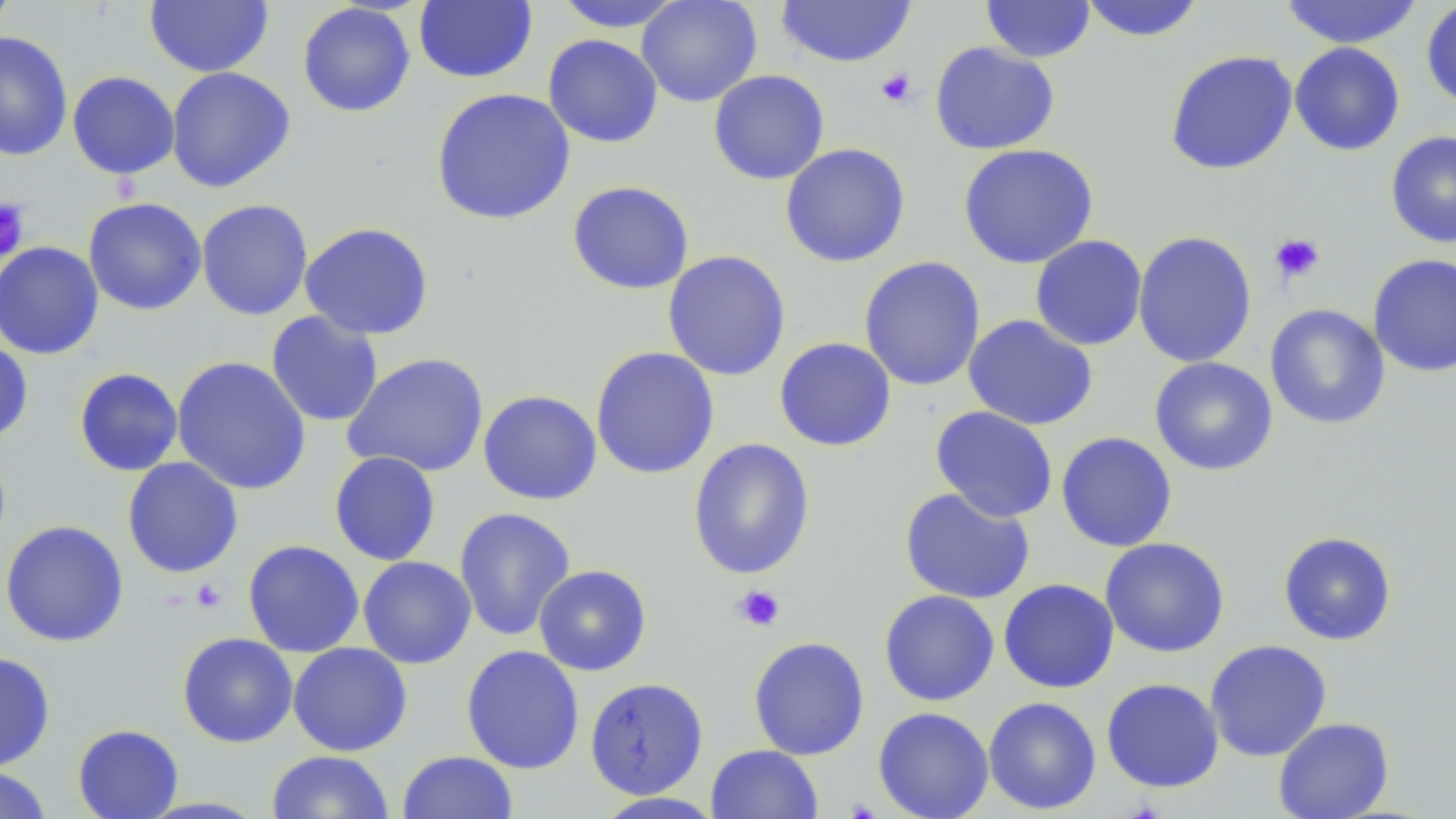 Approximate bounding boxes as (x1,y1)-(x2,y2) corner pairs in pixels. Uninfected red blood cell locations: (0,0)-(17,40), (636,0)-(763,107), (775,0)-(916,68), (1079,0)-(1206,42), (1277,0)-(1425,49), (144,1)-(274,77), (414,1)-(537,84), (553,1)-(688,33), (980,1)-(1096,63), (1421,1)-(1456,110), (297,3)-(416,118), (0,30)-(73,162), (543,34)-(664,148), (930,42)-(1060,155), (1289,42)-(1405,156), (1165,50)-(1298,175), (166,66)-(296,193), (708,69)-(830,185), (67,71)-(180,179), (431,88)-(576,225), (1386,130)-(1456,248), (780,143)-(911,267), (957,143)-(1099,269), (567,181)-(694,295), (82,197)-(207,315), (196,198)-(313,321), (299,222)-(434,340), (1133,230)-(1257,368), (1030,235)-(1147,351), (0,241)-(104,360), (662,250)-(791,381), (1368,253)-(1456,377), (859,256)-(986,391), (1265,304)-(1391,430), (266,311)-(383,427), (962,314)-(1098,430), (0,335)-(34,445), (774,337)-(897,452), (590,347)-(720,480), (342,352)-(489,478), (171,355)-(311,496), (1149,357)-(1278,476), (74,367)-(183,476), (478,390)-(602,505), (930,406)-(1058,522), (1055,431)-(1178,552), (687,437)-(816,580), (329,451)-(441,566), (122,457)-(244,578), (899,487)-(1036,605), (453,506)-(576,641), (0,520)-(129,647), (1278,531)-(1397,646), (1099,537)-(1230,658), (242,539)-(365,657), (358,556)-(476,669), (534,565)-(652,676), (998,578)-(1120,693), (878,590)-(1000,706), (177,632)-(298,748), (748,636)-(870,760), (1205,639)-(1332,762), (288,642)-(412,756), (461,645)-(584,774), (0,651)-(56,772), (584,677)-(709,799), (1101,678)-(1224,793), (983,696)-(1102,814), (872,706)-(994,819), (1273,717)-(1394,819), (72,724)-(184,819), (705,744)-(824,819), (266,750)-(394,818), (397,750)-(518,818), (0,766)-(52,819), (592,792)-(726,818). Platelet locations: (876,67)-(917,107), (0,198)-(30,262), (1269,232)-(1325,284), (190,578)-(227,612), (731,584)-(784,633). Slide-level diagnosis: no evidence of blood parasites. Light microscopy. One field of a larger specimen. Captured at 1000x magnification. May-Grünwald-Giemsa-stained preparation. Image is 1456×819 pixels. Thin blood smear.